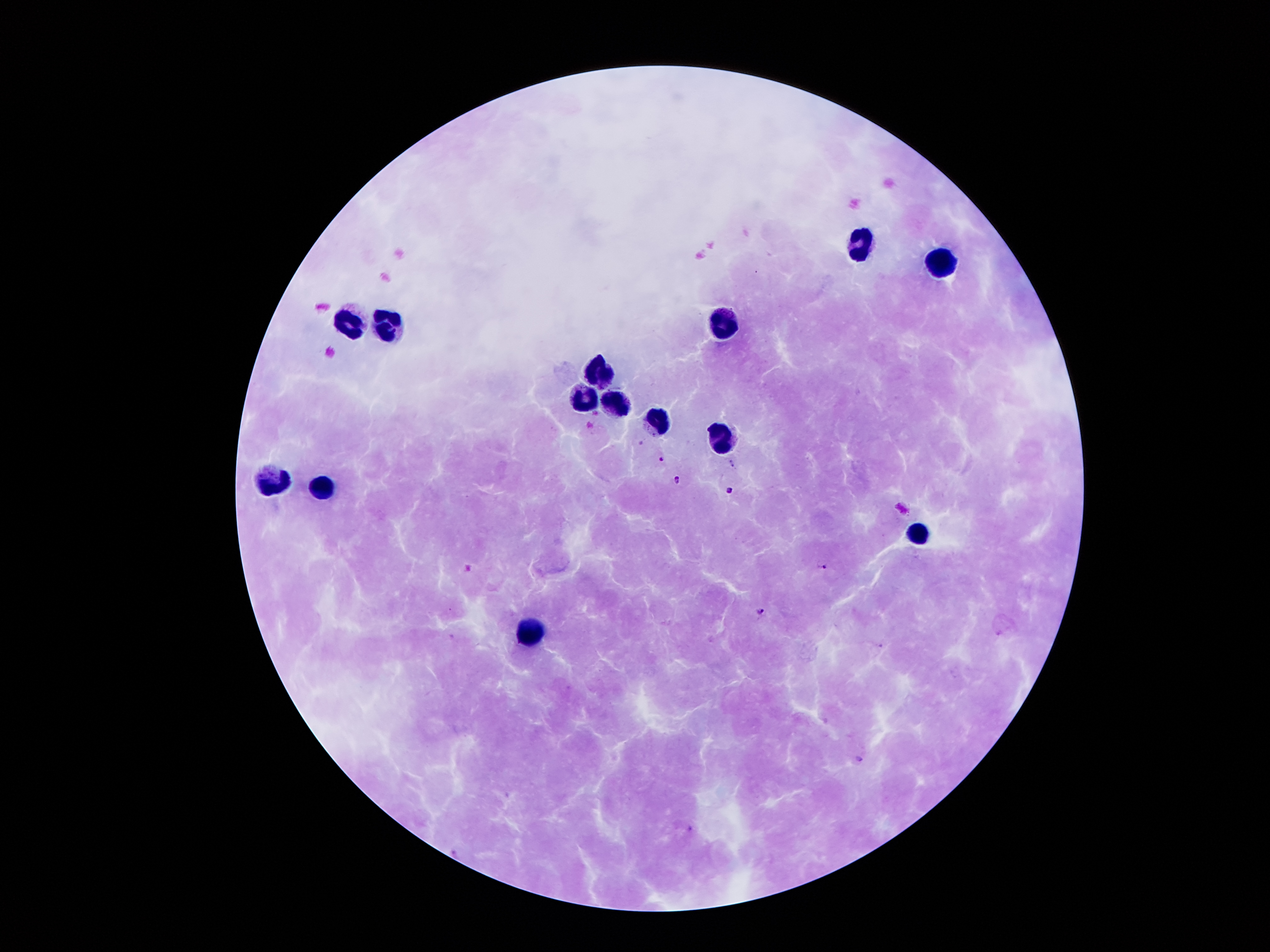 Approximate object centers, in pixels from the top-left corner. Malaria parasite locations: (x=641, y=443), (x=661, y=459), (x=731, y=463), (x=678, y=480), (x=730, y=490), (x=822, y=564), (x=759, y=611), (x=859, y=758). Leukocyte locations: (x=861, y=246), (x=938, y=264), (x=724, y=323), (x=346, y=324), (x=388, y=331), (x=599, y=374), (x=582, y=400), (x=615, y=402), (x=657, y=420), (x=724, y=436), (x=275, y=480), (x=323, y=489), (x=915, y=534), (x=529, y=634). Photographed through the microscope eyepiece with a smartphone camera. 100x magnification. Image is 1270×952 pixels. Single field of view. Giemsa stain. Patient malaria status: positive for Plasmodium falciparum. Thick blood film.